Report the malaria status of this cell.
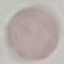

It is uninfected.

Giemsa-stained preparation. Thin blood smear. Cell patch, automatically extracted from a larger field of view and resized to 64 × 64 pixels. Acquired by smartphone through the microscope eyepiece.